State which cell type is depicted.
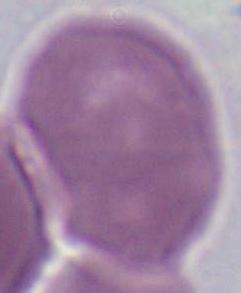

This is an erythrocyte.

Summary:
  - Modality: micrograph
  - Magnification: 1000x